Assess this cell for malaria.
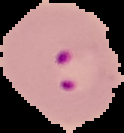

Parasitized.

{
  "image_type": "segmented cell region with the area outside set to black",
  "image_size": "124×133 pixels",
  "preparation": "thin blood smear"
}